Identify the preparation type.
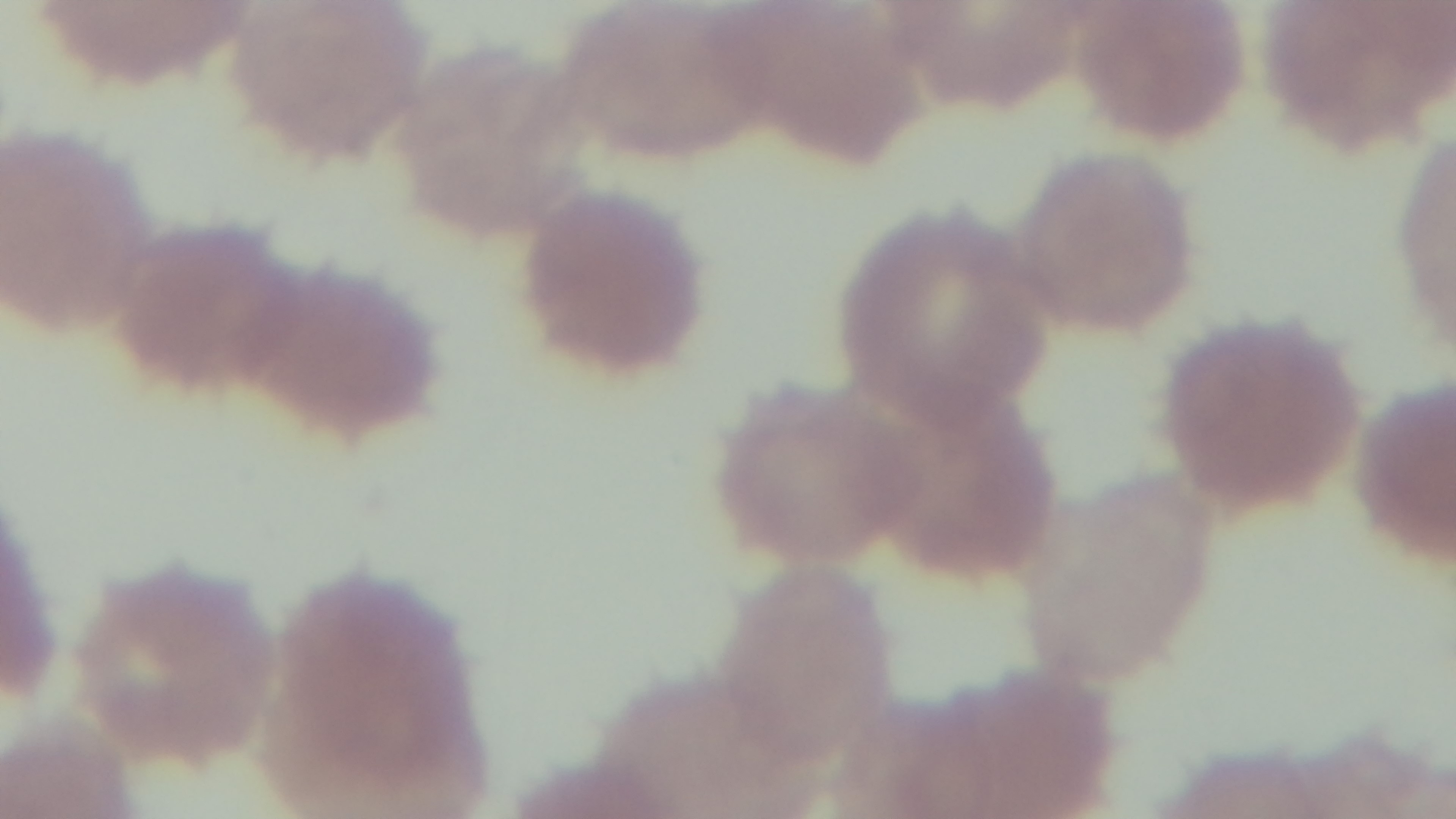

It is a thin blood film.

Giemsa stain. Light microscopy. One field from the slide. Malaria status: positive. Captured with a mounted 4K digital camera. 100x oil-immersion objective.